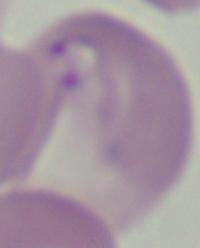

Summary:
  - Identification: Babesia
  - Magnification: 1000x
  - Modality: micrograph